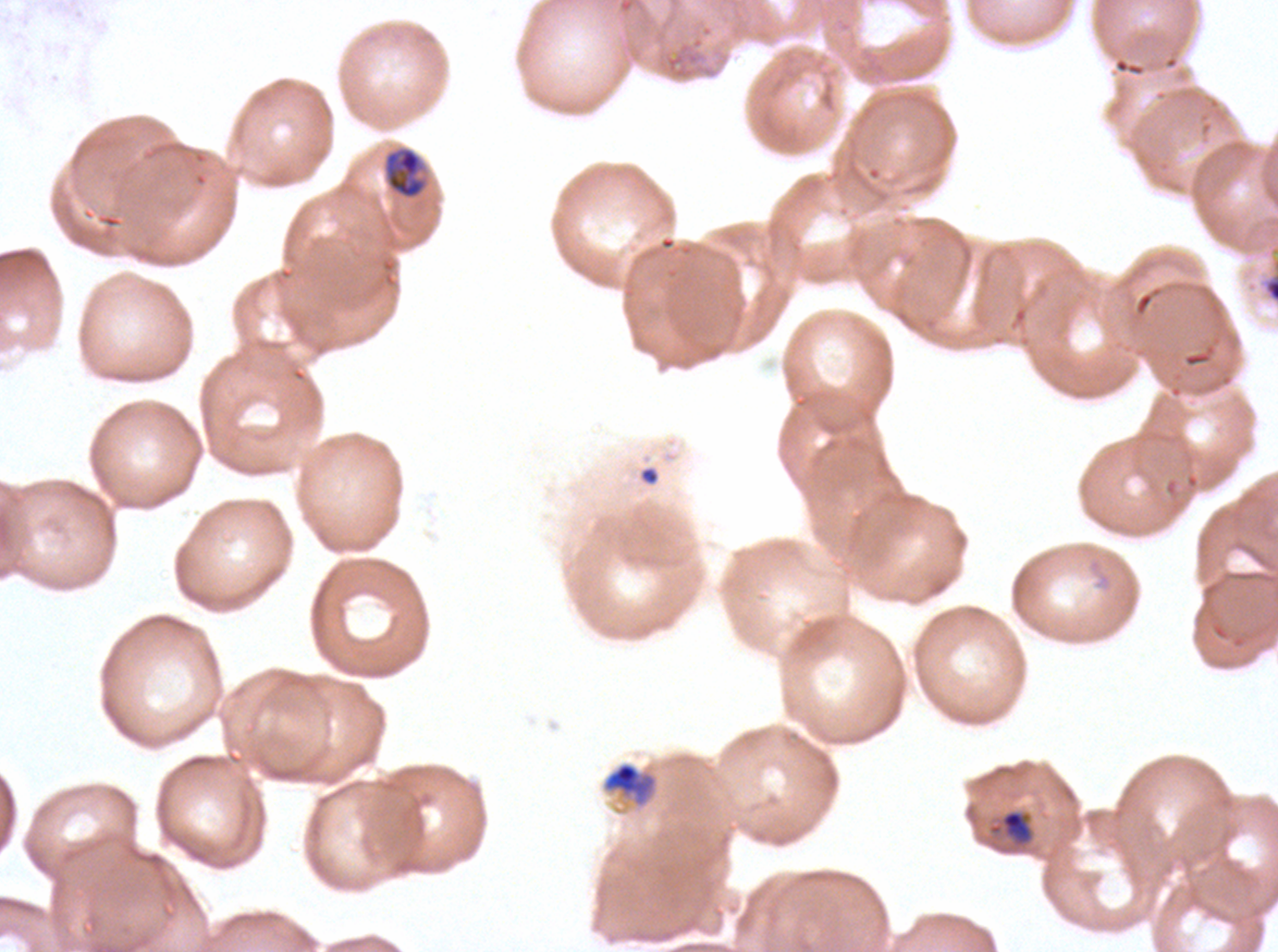

Approximate bounding boxes as (x1, y1, x2, y2) in pixels.
Summary:
  - Debris locations: (638, 465, 660, 486)
  - Late schizont locations: (1260, 256, 1277, 305)
  - Mid trophozoite locations: (383, 146, 427, 200), (601, 761, 659, 810)
  - Late-ring/early-trophozoite locations: (988, 809, 1034, 847)
  - Field of view: one sub-image of a larger composite
  - Stain: Giemsa
  - Life-cycle stages observed: late-ring/early-trophozoite, mid trophozoite, late schizont
  - Preparation: thin blood smear
  - Specimen: Plasmodium falciparum from a patient in The Gambia, cultured ex vivo for 24 to 48 hours
  - Image size: 1278×952 pixels